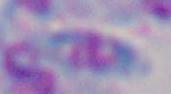

{
  "magnification": "1000x",
  "modality": "photomicrograph",
  "identification": "Toxoplasma gondii"
}